Identify the parasite.
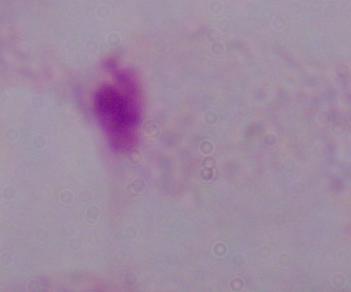
This is a trichomonad.

magnification = 1000x
modality = micrograph